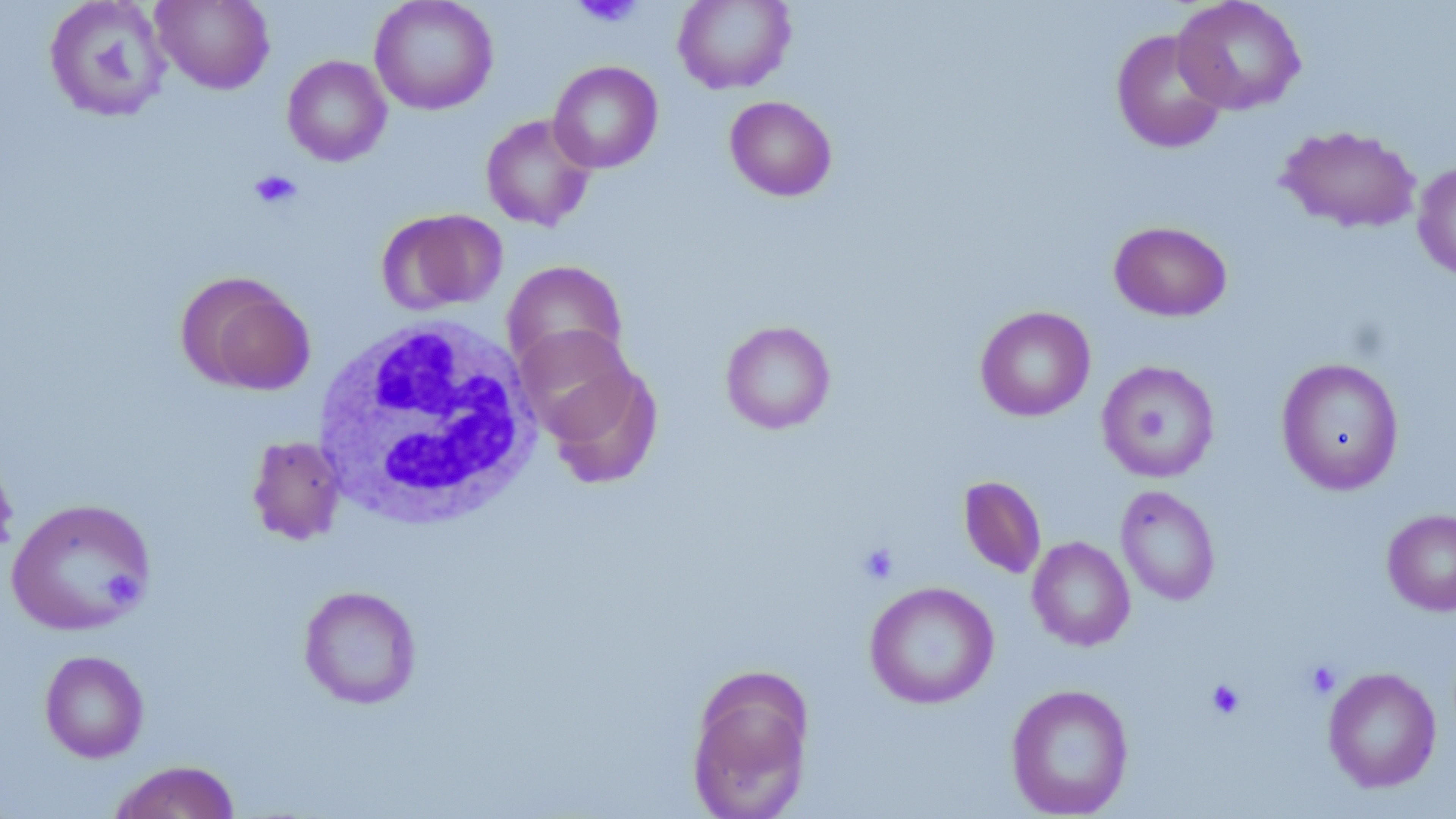

Summary:
  - Coordinate format: approximate bounding boxes as (x1, y1, x2, y2) in pixels
  - Platelet locations: (572, 0, 644, 29), (248, 169, 302, 210), (857, 541, 900, 586), (106, 569, 140, 602), (1304, 660, 1341, 699), (1206, 678, 1246, 720)
  - Uninfected red blood cell locations: (151, 0, 275, 94), (369, 0, 499, 115), (673, 0, 796, 94), (1172, 0, 1306, 115), (43, 1, 172, 124), (1111, 29, 1228, 153), (282, 55, 392, 166), (548, 61, 663, 173), (724, 96, 837, 201), (480, 113, 597, 231), (1277, 125, 1421, 233), (1412, 160, 1456, 281), (377, 208, 507, 314), (1109, 220, 1232, 321), (502, 260, 627, 374), (176, 271, 316, 396), (975, 305, 1095, 422), (720, 320, 836, 435), (515, 325, 638, 440), (1276, 357, 1404, 495), (1097, 360, 1220, 483), (544, 363, 663, 489), (247, 435, 346, 545), (0, 450, 19, 566), (958, 475, 1047, 579), (1115, 485, 1220, 606), (5, 497, 156, 636), (1382, 509, 1456, 615), (1027, 536, 1135, 651), (864, 580, 999, 709), (298, 585, 422, 709), (39, 649, 149, 763), (685, 665, 814, 819), (1323, 667, 1441, 793), (1006, 683, 1134, 818), (108, 759, 242, 819)
  - White blood cell locations: (312, 316, 543, 530)
  - Slide-level diagnosis: negative for blood parasites
  - Magnification: 1000x
  - Preparation: thin blood smear
  - Image size: 1456×819 pixels
  - Stain: May-Grünwald-Giemsa
  - Field of view: one of a larger specimen
  - Modality: light microscopy